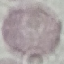
Summary:
  - Malaria status: uninfected
  - Capture: smartphone camera at the microscope eyepiece
  - Stain: Giemsa
  - Image type: cell patch, automatically extracted from a larger field of view and resized to 64 × 64 pixels
  - Preparation: thin smear